Identify the parasite.
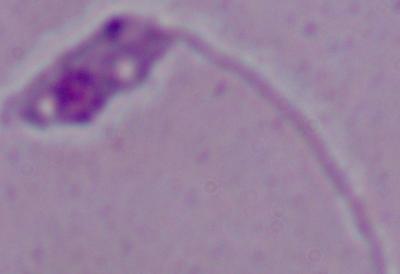

This is Leishmania.

Summary:
  - Modality: micrograph
  - Magnification: 1000x